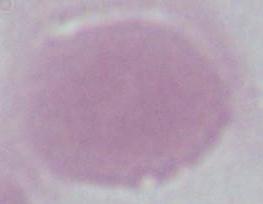
Summary:
  - Identification: red blood cell
  - Magnification: 1000x
  - Modality: photomicrograph